Mark where platelets are.
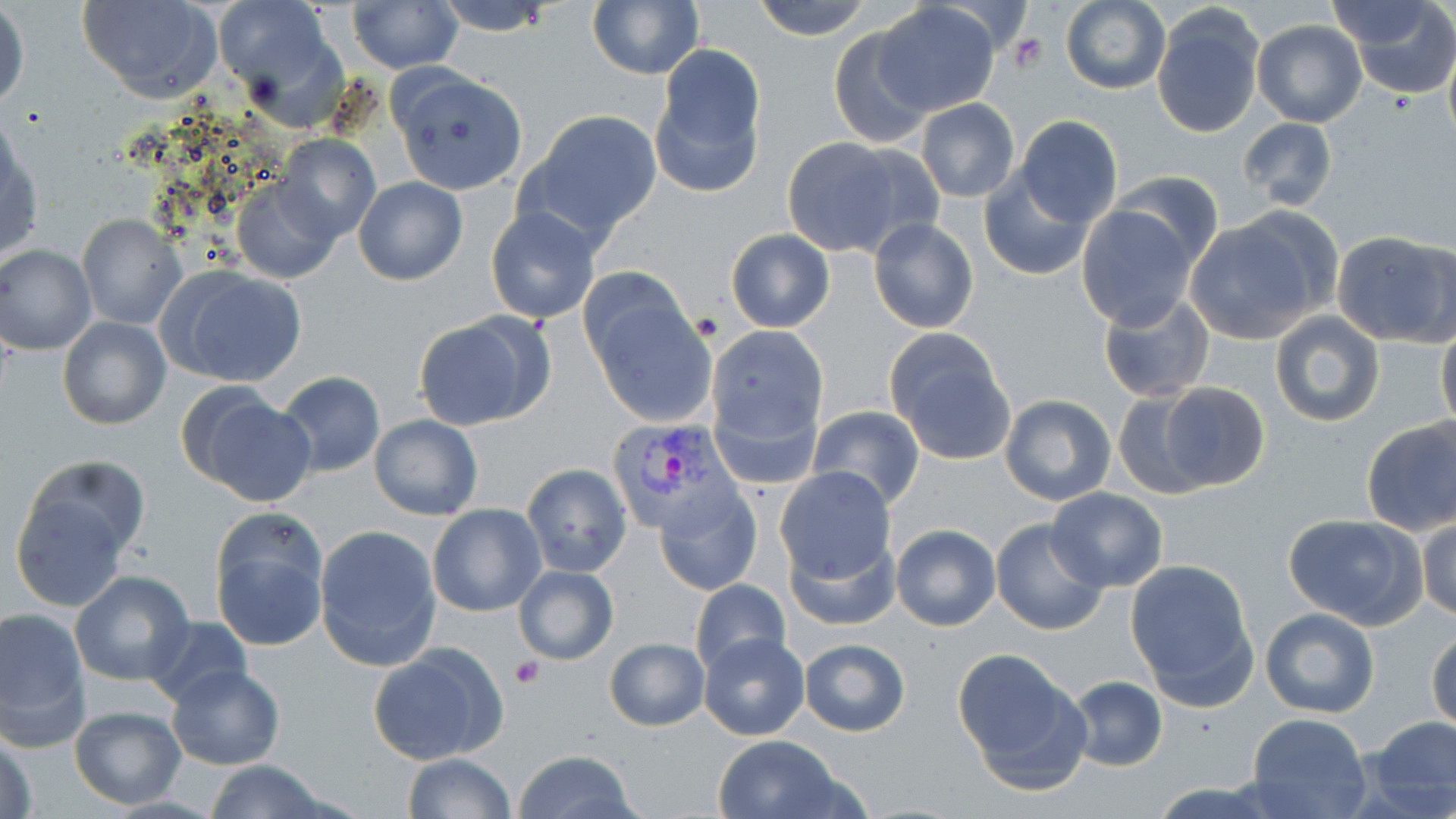
Approximate bounding boxes as named x1/y1/x2/y2 corners in pixels.
Platelets: (x1=1009, y1=33, x2=1048, y2=74), (x1=689, y1=309, x2=721, y2=343), (x1=510, y1=657, x2=545, y2=687).

Plasmodium vivax-infected red blood cell locations: (x1=604, y1=416, x2=733, y2=533). Uninfected red blood cell locations: (x1=77, y1=0, x2=223, y2=101), (x1=212, y1=0, x2=339, y2=108), (x1=431, y1=0, x2=559, y2=36), (x1=753, y1=0, x2=872, y2=42), (x1=1343, y1=0, x2=1455, y2=98), (x1=348, y1=1, x2=462, y2=73), (x1=587, y1=1, x2=703, y2=79), (x1=1327, y1=1, x2=1442, y2=52), (x1=1060, y1=2, x2=1169, y2=93), (x1=1, y1=3, x2=29, y2=110), (x1=874, y1=3, x2=997, y2=115), (x1=1153, y1=7, x2=1265, y2=139), (x1=1251, y1=20, x2=1366, y2=128), (x1=829, y1=25, x2=936, y2=149), (x1=650, y1=43, x2=767, y2=195), (x1=1442, y1=46, x2=1456, y2=152), (x1=391, y1=69, x2=528, y2=195), (x1=915, y1=99, x2=1021, y2=202), (x1=520, y1=109, x2=663, y2=245), (x1=1015, y1=116, x2=1123, y2=227), (x1=1236, y1=116, x2=1339, y2=211), (x1=1, y1=128, x2=42, y2=263), (x1=275, y1=134, x2=381, y2=242), (x1=782, y1=136, x2=928, y2=260), (x1=1113, y1=169, x2=1224, y2=270), (x1=978, y1=170, x2=1096, y2=281), (x1=231, y1=177, x2=340, y2=283), (x1=353, y1=177, x2=468, y2=285), (x1=1076, y1=203, x2=1197, y2=329), (x1=487, y1=206, x2=599, y2=325), (x1=77, y1=214, x2=187, y2=329), (x1=867, y1=216, x2=980, y2=334), (x1=1185, y1=217, x2=1325, y2=344), (x1=727, y1=229, x2=834, y2=332), (x1=1333, y1=232, x2=1454, y2=347), (x1=0, y1=245, x2=96, y2=354), (x1=162, y1=265, x2=307, y2=387), (x1=575, y1=269, x2=697, y2=383), (x1=1097, y1=290, x2=1217, y2=404), (x1=587, y1=297, x2=718, y2=427), (x1=1269, y1=310, x2=1385, y2=427), (x1=413, y1=312, x2=552, y2=431), (x1=58, y1=317, x2=172, y2=431), (x1=1436, y1=322, x2=1456, y2=433), (x1=707, y1=325, x2=828, y2=450), (x1=885, y1=332, x2=1015, y2=462), (x1=276, y1=371, x2=386, y2=477), (x1=1155, y1=382, x2=1273, y2=493), (x1=177, y1=384, x2=317, y2=506), (x1=1112, y1=391, x2=1212, y2=499), (x1=1000, y1=394, x2=1116, y2=507), (x1=807, y1=404, x2=925, y2=510), (x1=369, y1=415, x2=485, y2=521), (x1=1360, y1=417, x2=1456, y2=536), (x1=24, y1=456, x2=150, y2=566), (x1=520, y1=464, x2=633, y2=579), (x1=774, y1=466, x2=898, y2=585), (x1=655, y1=484, x2=762, y2=596), (x1=10, y1=487, x2=134, y2=612), (x1=1046, y1=488, x2=1168, y2=592), (x1=427, y1=502, x2=546, y2=617), (x1=1283, y1=513, x2=1425, y2=630), (x1=1417, y1=513, x2=1456, y2=622), (x1=210, y1=515, x2=329, y2=650), (x1=991, y1=518, x2=1108, y2=635), (x1=314, y1=524, x2=441, y2=668), (x1=891, y1=524, x2=1000, y2=631), (x1=783, y1=530, x2=901, y2=632), (x1=1123, y1=558, x2=1257, y2=700), (x1=512, y1=565, x2=620, y2=665), (x1=69, y1=571, x2=195, y2=688), (x1=691, y1=578, x2=791, y2=676), (x1=0, y1=606, x2=89, y2=741), (x1=1259, y1=606, x2=1380, y2=717), (x1=143, y1=616, x2=252, y2=708), (x1=1427, y1=627, x2=1456, y2=735), (x1=700, y1=632, x2=810, y2=741), (x1=605, y1=637, x2=708, y2=731), (x1=800, y1=638, x2=910, y2=737), (x1=369, y1=642, x2=508, y2=766), (x1=953, y1=653, x2=1089, y2=788), (x1=166, y1=664, x2=284, y2=769), (x1=1067, y1=675, x2=1165, y2=772), (x1=69, y1=706, x2=186, y2=808), (x1=1244, y1=712, x2=1371, y2=819), (x1=1365, y1=715, x2=1456, y2=816), (x1=2, y1=726, x2=39, y2=819), (x1=715, y1=735, x2=844, y2=819), (x1=512, y1=750, x2=639, y2=819), (x1=401, y1=752, x2=515, y2=819), (x1=203, y1=760, x2=331, y2=819). Slide-level diagnosis: Plasmodium vivax. One field of a larger specimen. Optical microscopy. Thin blood smear. Captured at 1000x magnification. May-Grünwald-Giemsa-stained preparation. Image is 1456×819 pixels.